Assess this cell for malaria.
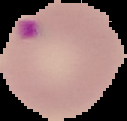

Parasitized.

Summary:
  - Preparation: thin blood smear
  - Image type: cell region segmented out of the field of view; surrounding area masked to black
  - Image size: 127×121 pixels